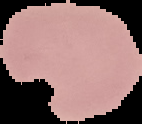

image size = 142×124 pixels
image type = cell region segmented out of the field of view; surrounding area masked to black
preparation = thin blood film
malaria status = uninfected